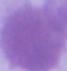

Summary:
  - Identification: red blood cell
  - Modality: photomicrograph
  - Magnification: 1000x